Describe the morphology of the red blood cells.
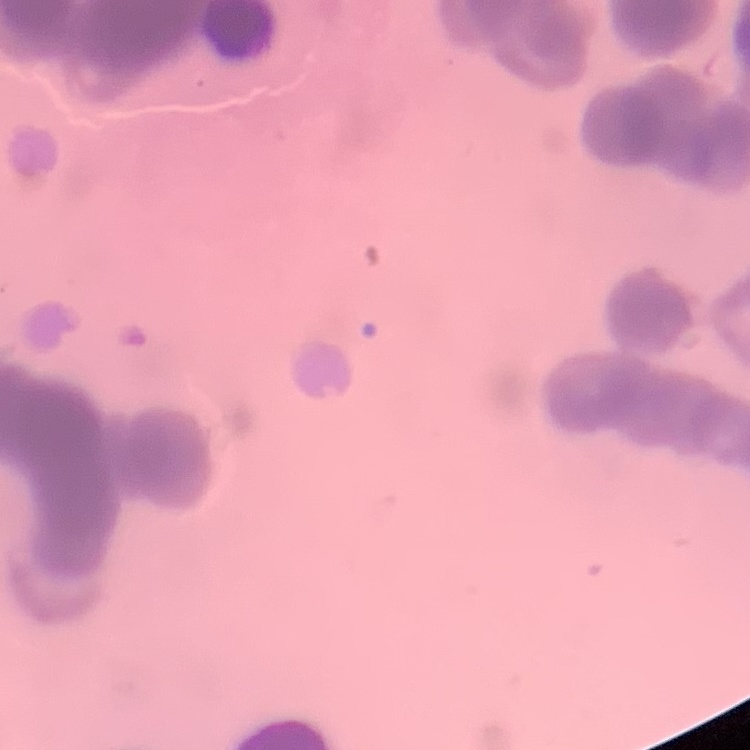
Rouleaux formation.

stain: Field's or Giemsa
image_type: one tile cut from a larger photomicrograph
preparation: thin blood film